Give the preparation type.
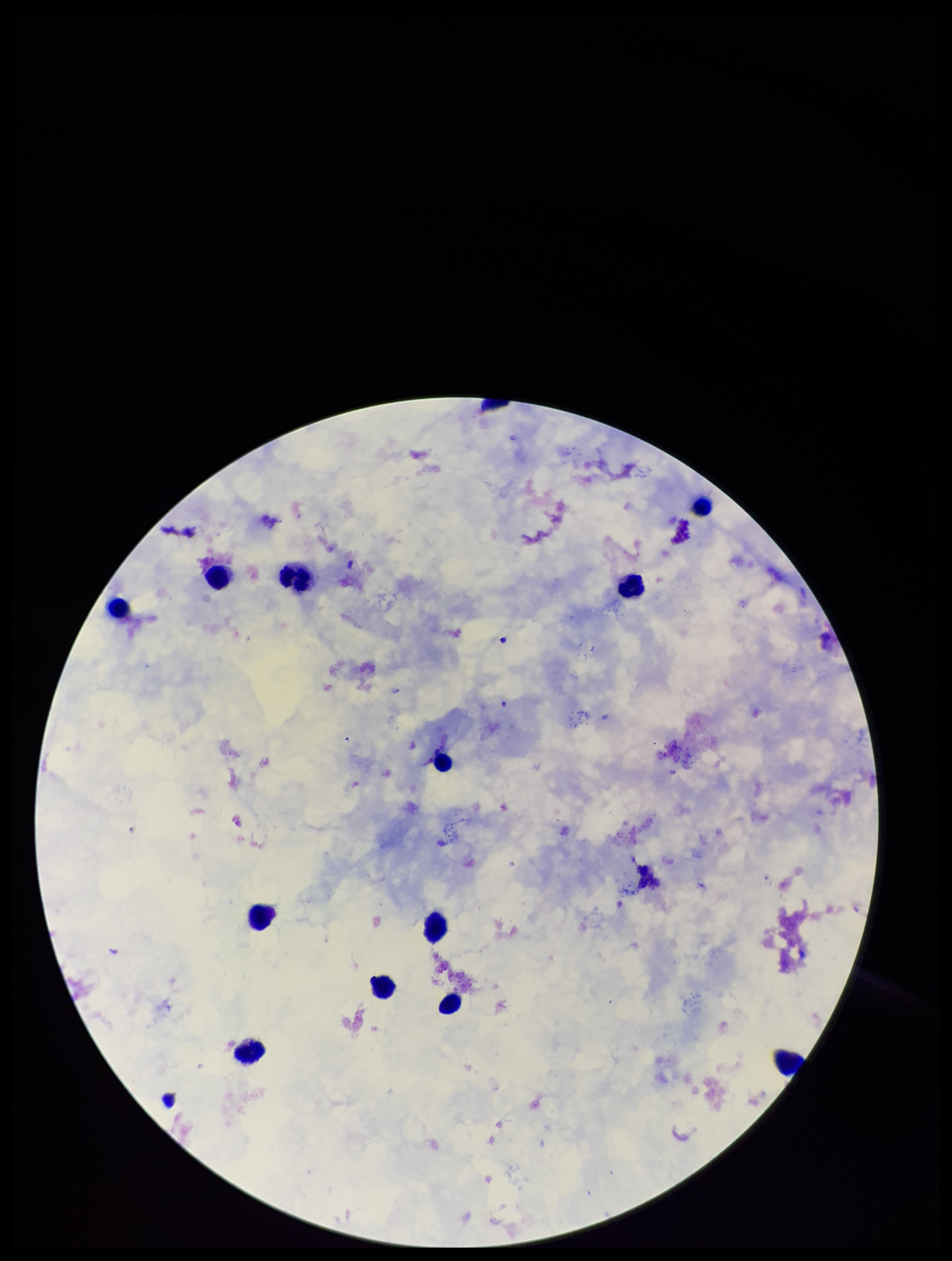

Thick.

Summary:
  - Parasite count: 0
  - Capture: smartphone photograph through the microscope eyepiece
  - Plasmodium parasites: none detected
  - Patient malaria status: negative
  - Leukocyte count: 12
  - Stain: Giemsa
  - Field of view: one from this slide
  - Image size: 952×1261 pixels